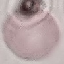
{
  "malaria_status": "uninfected",
  "capture": "smartphone through the microscope eyepiece",
  "preparation": "thin blood smear",
  "stain": "Giemsa",
  "image_type": "cell patch, automatically extracted from a larger field of view and resized to 64 × 64 pixels"
}